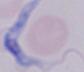

A trypanosome is seen. Micrograph. 1000x magnification.